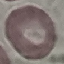
Result: no malaria parasites detected. Automatically extracted cell patch, resized to 64 × 64 pixels. Giemsa stain. Photographed with a smartphone camera at the microscope eyepiece. Thin smear of blood.